Describe the morphology of the red blood cells.
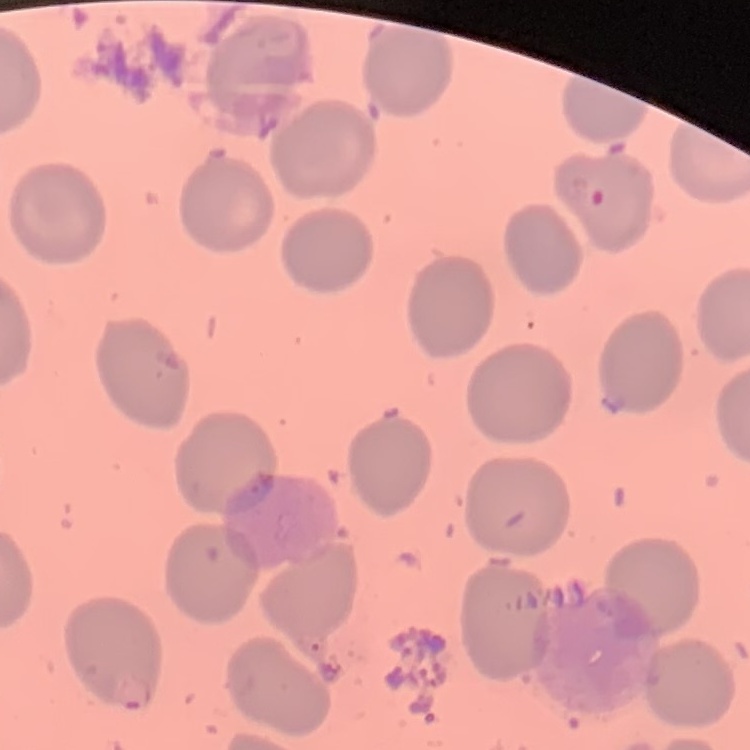
They show no rouleaux formation.

Summary:
  - Image type: square crop of a larger photomicrograph
  - Stain: Field's or Giemsa
  - Preparation: thin blood film